Give the extent of all uninfected red blood cells.
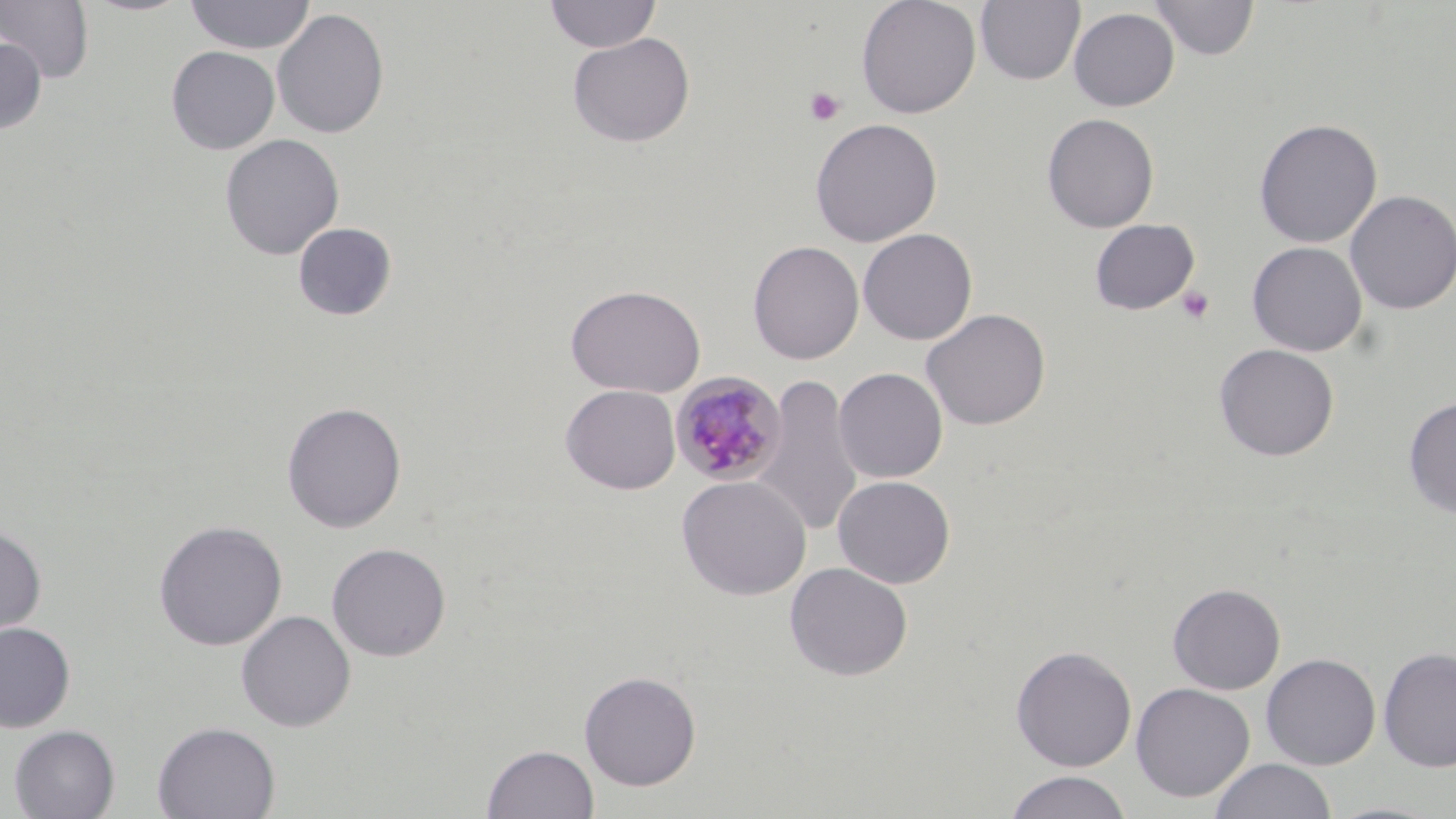

Approximate bounding boxes as [x1, y1, x2, y2] in pixels.
Uninfected red blood cells: [0, 0, 95, 84], [183, 0, 316, 54], [543, 0, 662, 54], [856, 0, 981, 118], [975, 0, 1085, 85], [1150, 0, 1259, 61], [1068, 7, 1179, 111], [272, 8, 390, 140], [567, 32, 696, 148], [0, 37, 47, 136], [166, 45, 280, 154], [1042, 113, 1159, 233], [809, 117, 943, 247], [1253, 118, 1382, 249], [220, 134, 344, 260], [1344, 190, 1456, 315], [1089, 219, 1199, 315], [292, 222, 397, 321], [858, 228, 978, 345], [747, 241, 864, 364], [1247, 241, 1368, 357], [565, 284, 706, 398], [922, 308, 1051, 431], [1214, 343, 1339, 462], [834, 367, 948, 483], [755, 372, 862, 540], [560, 384, 681, 494], [1403, 397, 1456, 518], [281, 401, 407, 533], [676, 475, 812, 600], [832, 475, 955, 588], [153, 519, 287, 651], [0, 524, 47, 645], [326, 542, 452, 662], [784, 562, 913, 681], [1168, 583, 1286, 694], [236, 610, 356, 732], [0, 622, 76, 733], [4, 624, 90, 818], [1010, 644, 1137, 772], [1378, 646, 1456, 773], [1261, 653, 1381, 770], [579, 670, 702, 791], [1130, 681, 1255, 803], [152, 721, 281, 819], [8, 724, 120, 819], [483, 744, 599, 819], [1208, 758, 1337, 819], [1003, 770, 1133, 819].

Summary:
  - Plasmodium malariae-infected red blood cell locations: [671, 373, 787, 486]
  - Platelet locations: [804, 86, 846, 127], [1176, 285, 1216, 325]
  - Slide-level diagnosis: Plasmodium malariae
  - Image size: 1456×819 pixels
  - Preparation: thin blood smear
  - Field of view: one of a larger specimen
  - Modality: light microscopy
  - Stain: May-Grünwald-Giemsa
  - Magnification: 1000x